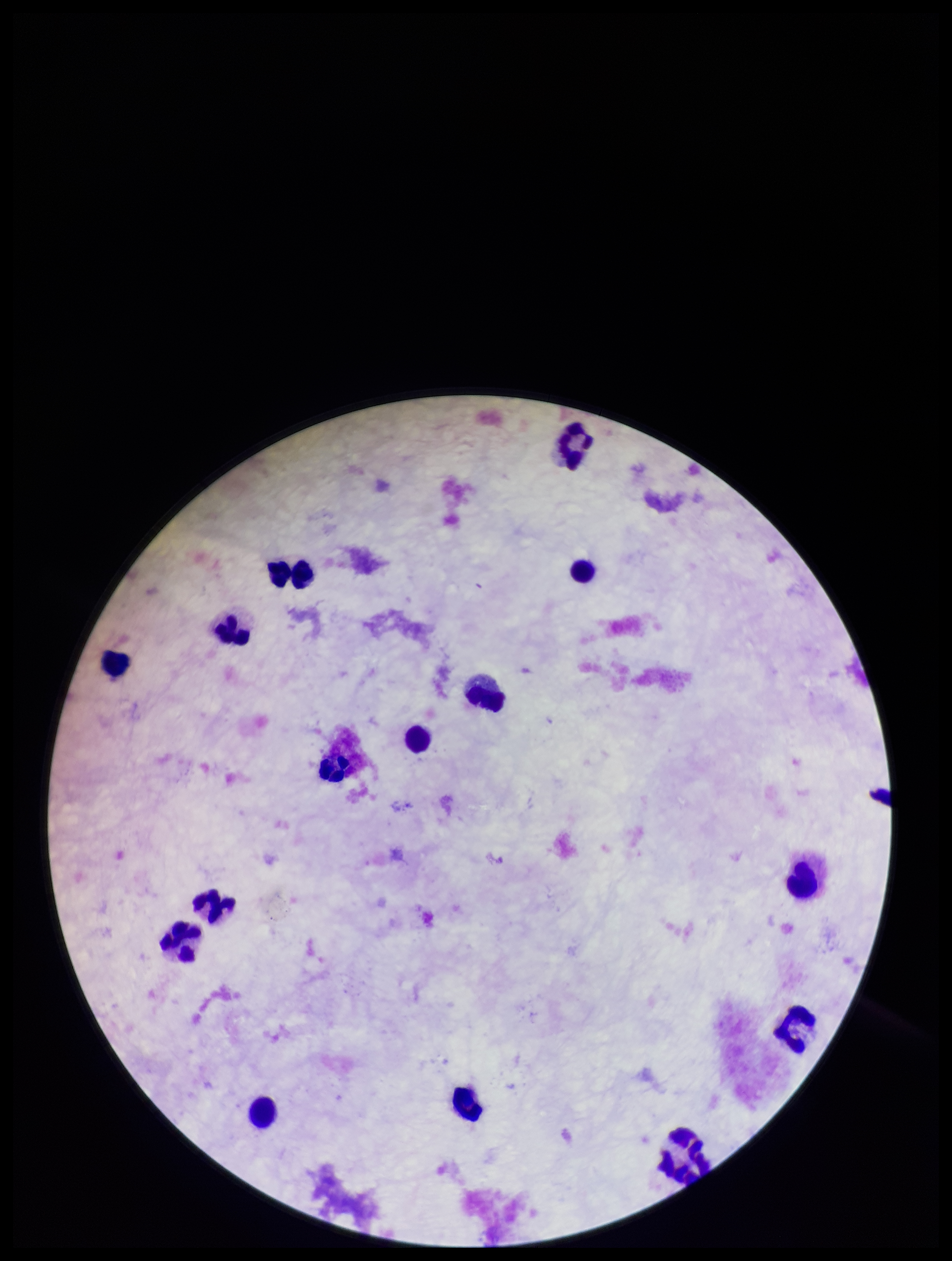

Summary:
  - Parasite count: 0
  - Stain: Giemsa
  - Leukocyte count: 15
  - Image size: 952×1261 pixels
  - Preparation: thick blood smear
  - Field of view: single
  - Plasmodium parasites: none detected
  - Capture: smartphone photograph through the microscope eyepiece
  - Patient malaria status: negative